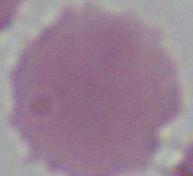

Captured at 1000x magnification. Photomicrograph. A red blood cell is shown.